Classify this cell by malaria status.
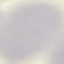
It is uninfected.

Thin smear of blood. Automatically extracted cell patch, resized to 64 × 64 pixels. Acquired by smartphone through the microscope eyepiece. Giemsa stain.